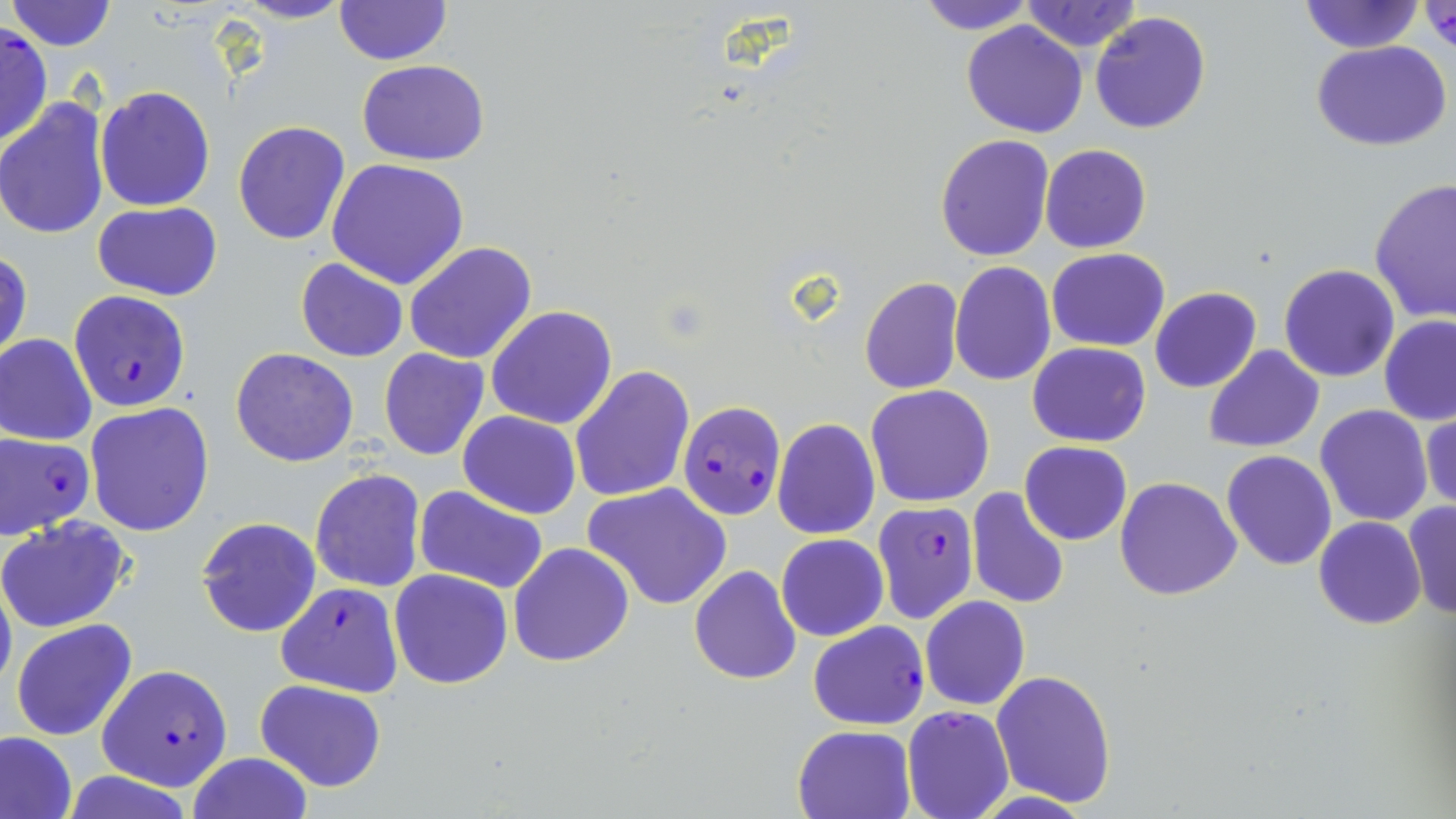
slide_level_diagnosis: Plasmodium falciparum
image_size: 1456×819 pixels
preparation: thin blood film
magnification: 1000x
modality: optical microscopy
uninfected_red_blood_cell_locations: 'approximate bounding boxes as named x1/y1/x2/y2 corners in pixels: (x1=233, y1=0, x2=353, y2=24), (x1=918, y1=0, x2=1035, y2=34), (x1=1019, y1=0, x2=1142, y2=53), (x1=1298, y1=0, x2=1423, y2=55), (x1=5, y1=1, x2=119, y2=51), (x1=333, y1=1, x2=453, y2=66), (x1=1418, y1=2, x2=1455, y2=54), (x1=1090, y1=10, x2=1212, y2=133), (x1=961, y1=21, x2=1088, y2=138), (x1=0, y1=25, x2=51, y2=148), (x1=1311, y1=41, x2=1454, y2=152), (x1=356, y1=59, x2=490, y2=166), (x1=94, y1=86, x2=215, y2=211), (x1=0, y1=99, x2=110, y2=241), (x1=233, y1=119, x2=351, y2=246), (x1=935, y1=135, x2=1054, y2=261), (x1=1040, y1=144, x2=1151, y2=254), (x1=327, y1=158, x2=472, y2=289), (x1=1368, y1=178, x2=1456, y2=325), (x1=93, y1=203, x2=222, y2=302), (x1=404, y1=240, x2=538, y2=365), (x1=1, y1=249, x2=32, y2=366), (x1=1046, y1=249, x2=1170, y2=351), (x1=295, y1=258, x2=409, y2=362), (x1=949, y1=261, x2=1057, y2=386), (x1=1279, y1=264, x2=1401, y2=383), (x1=858, y1=276, x2=963, y2=395), (x1=1151, y1=287, x2=1261, y2=394), (x1=486, y1=305, x2=619, y2=429), (x1=1379, y1=314, x2=1456, y2=425), (x1=1, y1=334, x2=97, y2=446), (x1=1026, y1=342, x2=1151, y2=447), (x1=1205, y1=345, x2=1325, y2=453), (x1=230, y1=346, x2=360, y2=468), (x1=378, y1=348, x2=490, y2=461), (x1=569, y1=365, x2=693, y2=505), (x1=865, y1=384, x2=994, y2=506), (x1=85, y1=404, x2=216, y2=537), (x1=1315, y1=405, x2=1434, y2=528), (x1=1421, y1=406, x2=1455, y2=517), (x1=458, y1=411, x2=582, y2=519), (x1=772, y1=418, x2=880, y2=539), (x1=1019, y1=441, x2=1133, y2=546), (x1=1221, y1=449, x2=1337, y2=569), (x1=310, y1=468, x2=426, y2=594), (x1=1115, y1=476, x2=1242, y2=600), (x1=584, y1=482, x2=733, y2=611), (x1=414, y1=486, x2=548, y2=594), (x1=966, y1=486, x2=1070, y2=609), (x1=1403, y1=502, x2=1456, y2=620), (x1=0, y1=515, x2=133, y2=635), (x1=196, y1=516, x2=321, y2=638), (x1=1313, y1=516, x2=1425, y2=630), (x1=775, y1=533, x2=888, y2=641), (x1=508, y1=543, x2=634, y2=667), (x1=688, y1=565, x2=801, y2=685), (x1=389, y1=569, x2=512, y2=689), (x1=0, y1=572, x2=16, y2=701), (x1=920, y1=595, x2=1030, y2=711), (x1=11, y1=619, x2=138, y2=741), (x1=991, y1=670, x2=1117, y2=807), (x1=254, y1=679, x2=387, y2=791), (x1=793, y1=726, x2=915, y2=818), (x1=0, y1=730, x2=77, y2=819), (x1=186, y1=753, x2=313, y2=819)'
field_of_view: one of a larger specimen
plasmodium_falciparum_infected_red_blood_cell_locations: 'approximate bounding boxes as named x1/y1/x2/y2 corners in pixels: (x1=69, y1=290, x2=191, y2=413), (x1=678, y1=400, x2=784, y2=522), (x1=0, y1=431, x2=95, y2=538), (x1=873, y1=500, x2=979, y2=623), (x1=274, y1=580, x2=405, y2=697), (x1=808, y1=620, x2=930, y2=730), (x1=98, y1=664, x2=233, y2=791), (x1=901, y1=704, x2=1013, y2=819)'
stain: May-Grünwald-Giemsa